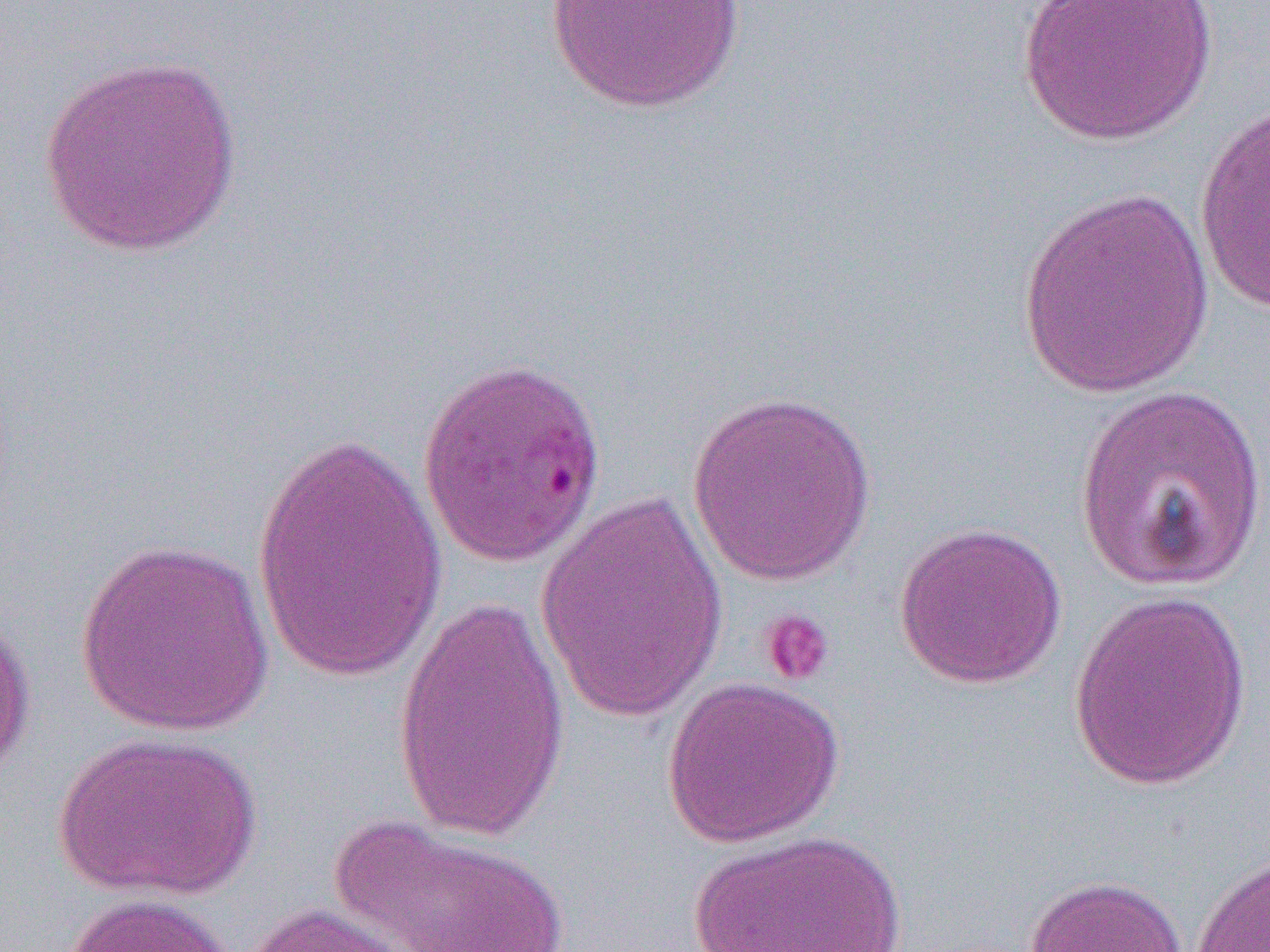
Approximate bounding boxes as (x1, y1, x2, y2) in pixels. Uninfected red blood cell locations: (546, 0, 746, 113), (1018, 0, 1218, 146), (36, 52, 244, 258), (1194, 99, 1270, 314), (1016, 188, 1217, 398), (1074, 382, 1268, 593), (687, 390, 878, 585), (249, 424, 449, 686), (535, 488, 730, 724), (892, 520, 1067, 689), (74, 538, 276, 737), (1068, 590, 1252, 791), (391, 593, 573, 842), (0, 608, 37, 786), (660, 675, 844, 848), (52, 730, 262, 901), (327, 814, 571, 952), (689, 829, 909, 952), (1190, 848, 1270, 952), (1023, 874, 1188, 952), (60, 893, 236, 952), (236, 901, 426, 952). Platelet locations: (758, 608, 836, 688). Slide-level diagnosis: Plasmodium falciparum. 1000x magnification. Thin blood smear. Image is 1270×952 pixels. Optical microscopy. One field of a larger specimen.